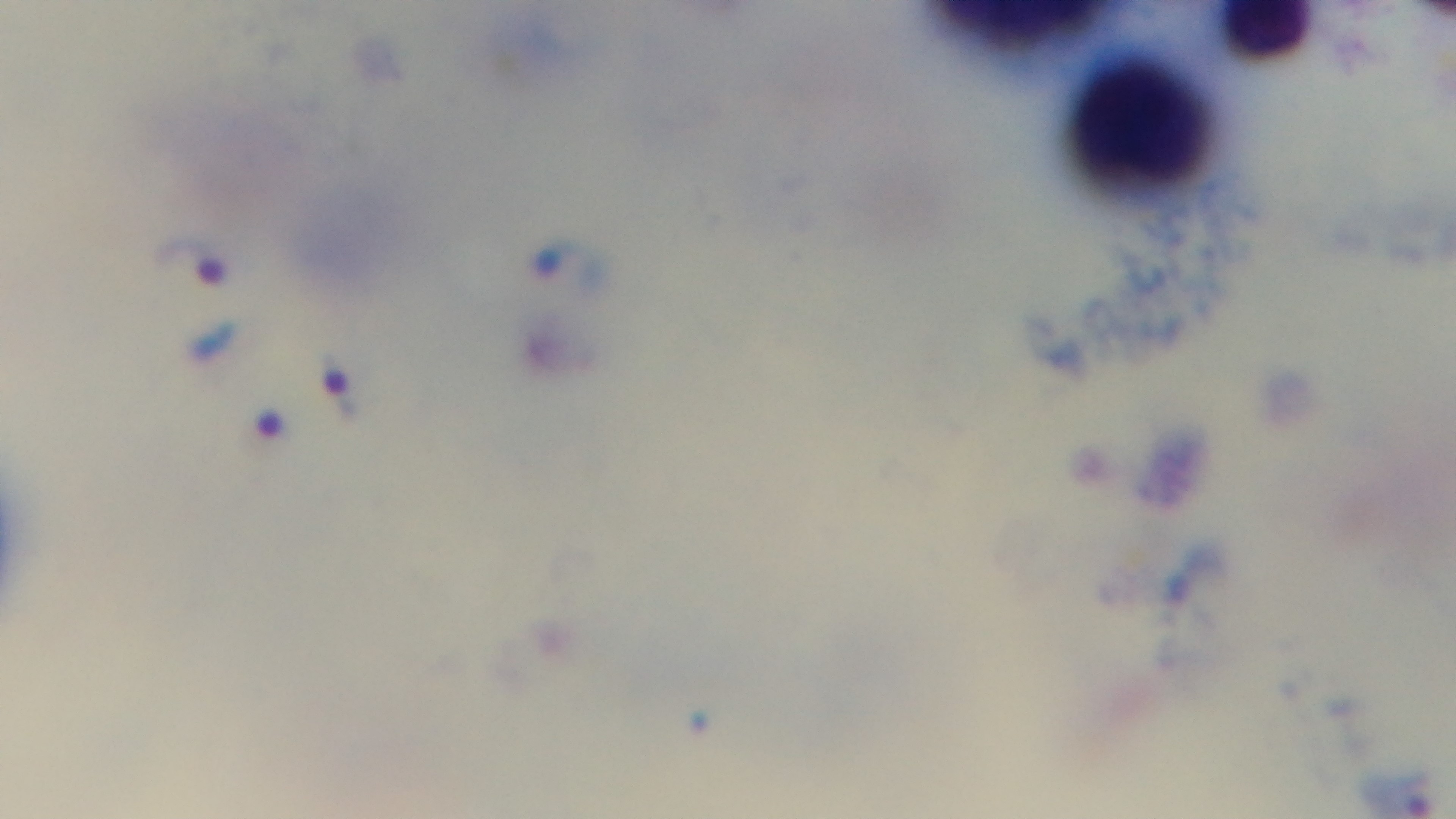
Summary:
  - Stain: Giemsa
  - Capture: mounted 4K digital camera
  - Malaria status: infected
  - Objective: 100x oil immersion
  - Modality: light microscopy
  - Preparation: thick smear
  - Field of view: one from the slide